Comment on the morphology of the red blood cells.
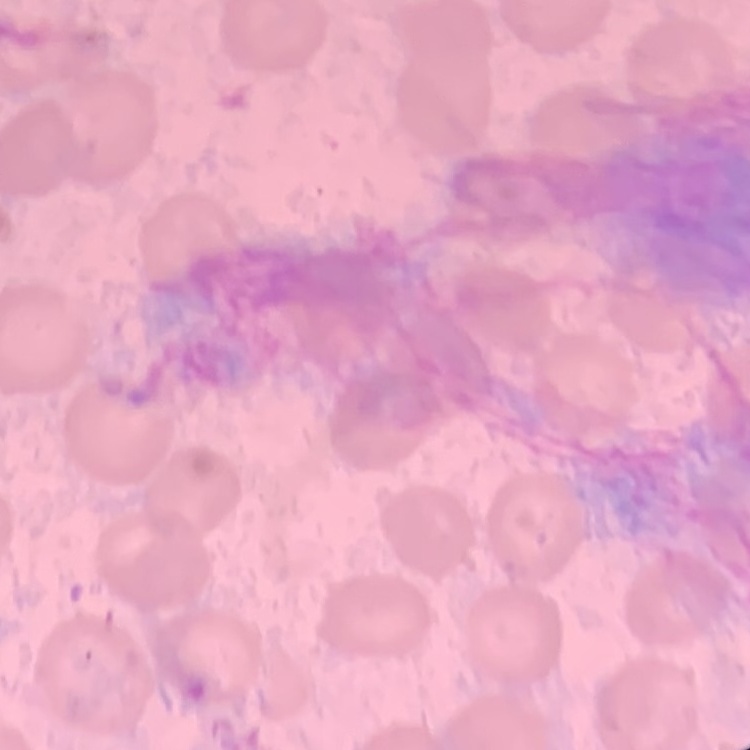
They show no rouleaux formation.

Summary:
  - Preparation: thin blood smear
  - Stain: Field's or Giemsa
  - Image type: one tile cut from a larger photomicrograph